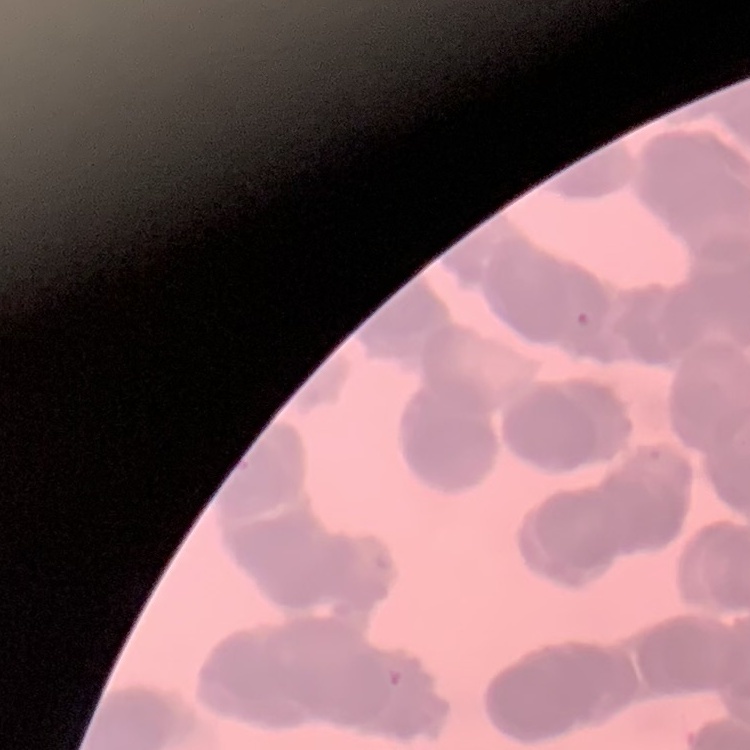

Summary:
  - Red blood cell morphology: rouleaux formation
  - Image type: square crop of a larger photomicrograph
  - Preparation: thin peripheral smear
  - Stain: Field's or Giemsa